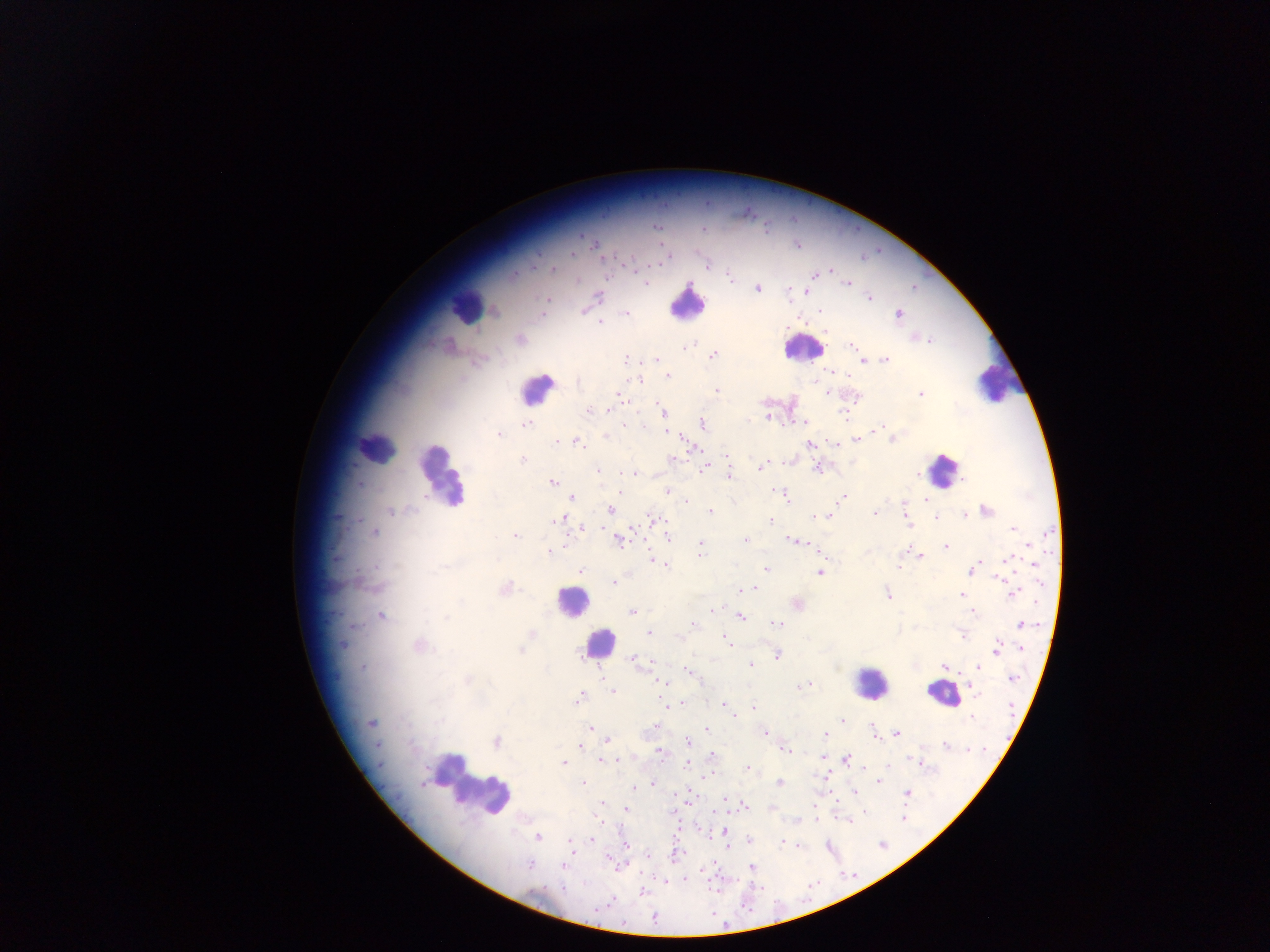
Approximate centers as [x, y] in pixels. Leukocyte locations: [693, 306], [466, 313], [803, 350], [990, 379], [935, 469], [440, 480], [571, 604], [599, 642], [875, 680], [938, 702], [468, 788]. Malaria parasite locations: [656, 228], [703, 229], [583, 236], [591, 242], [595, 246], [798, 247], [600, 254], [573, 258], [664, 261], [707, 265], [628, 266], [552, 267], [828, 270], [729, 277], [645, 281], [847, 282], [690, 286], [758, 289], [788, 289], [914, 289], [805, 290], [598, 296], [869, 297], [584, 312], [626, 312], [494, 313], [897, 313], [489, 314], [820, 314], [599, 323], [928, 340], [852, 344], [687, 345], [712, 354], [626, 358], [654, 359], [885, 360], [861, 361], [668, 377], [637, 381], [545, 382], [718, 392], [828, 392], [922, 392], [618, 394], [590, 409], [662, 409], [844, 414], [662, 415], [765, 418], [702, 423], [805, 423], [626, 424], [528, 425], [886, 425], [880, 428], [666, 433], [497, 435], [607, 435], [894, 439], [557, 441], [578, 441], [857, 441], [811, 445], [690, 446], [367, 451], [672, 457], [728, 458], [523, 460], [767, 463], [787, 463], [956, 463], [760, 467], [705, 468], [817, 468], [727, 469], [597, 471], [637, 474], [918, 474], [730, 475], [962, 480], [552, 482], [362, 483], [776, 489], [666, 490], [572, 497], [844, 497], [786, 498], [926, 501], [390, 510], [610, 510], [986, 510], [709, 511], [875, 512], [965, 515], [830, 516], [909, 516], [650, 518], [813, 518], [556, 519], [359, 520], [771, 520], [906, 521], [935, 521], [577, 526], [1011, 529], [376, 533], [515, 534], [618, 536], [668, 538], [746, 540], [620, 541], [793, 541], [946, 545], [1029, 546], [649, 548], [702, 548], [549, 551], [702, 553], [651, 555], [922, 557], [1008, 559], [978, 560], [901, 564], [666, 566], [1036, 566], [765, 567], [972, 567], [581, 568], [971, 573], [819, 574], [998, 579], [612, 582], [355, 583], [366, 587], [505, 589], [748, 589], [741, 590], [886, 590], [1015, 592], [962, 593], [887, 595], [712, 609], [631, 613], [973, 613], [381, 614], [446, 616], [742, 616], [351, 624], [776, 624], [1021, 624], [649, 632], [531, 633], [963, 636], [679, 637], [726, 641], [418, 645], [342, 647], [1022, 647], [520, 651], [996, 651], [628, 655], [583, 656], [777, 656], [633, 658], [749, 663], [635, 665], [837, 667], [363, 668], [944, 668], [976, 668], [690, 670], [692, 673], [467, 678], [1013, 678], [812, 684], [666, 685], [805, 685], [797, 686], [613, 692], [976, 692], [579, 697], [722, 702], [685, 703], [668, 705], [753, 708], [671, 709], [842, 717], [732, 718], [973, 718], [372, 724], [654, 725], [590, 726], [873, 728], [706, 729], [765, 733], [898, 734], [824, 736], [608, 740], [687, 741], [378, 743], [496, 743], [946, 745], [581, 746], [786, 751], [661, 752], [711, 753], [821, 758], [846, 758], [912, 758], [602, 760], [608, 761], [618, 761], [687, 763], [563, 764], [748, 768], [706, 775], [423, 783], [582, 783], [654, 783], [779, 783], [878, 783], [633, 787], [854, 793], [907, 793], [602, 804], [746, 806], [625, 809], [771, 811], [902, 820], [815, 821], [849, 821], [538, 838], [591, 838], [623, 841], [749, 841], [569, 842], [781, 842], [797, 844], [727, 845], [571, 851], [673, 856], [607, 860], [527, 865], [749, 867], [706, 871], [686, 879], [642, 891], [606, 902]. Single field of view. Sample from Ghana. Image is 1270×952 pixels. Mobile-phone photograph taken through the microscope. Thick blood film.